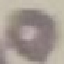

Summary:
  - Result: no malaria parasites detected
  - Image type: cell patch, automatically extracted from a larger field of view and resized to 64 × 64 pixels
  - Preparation: thin smear
  - Capture: smartphone camera at the microscope eyepiece
  - Stain: Giemsa